Look for parasitized red blood cells.
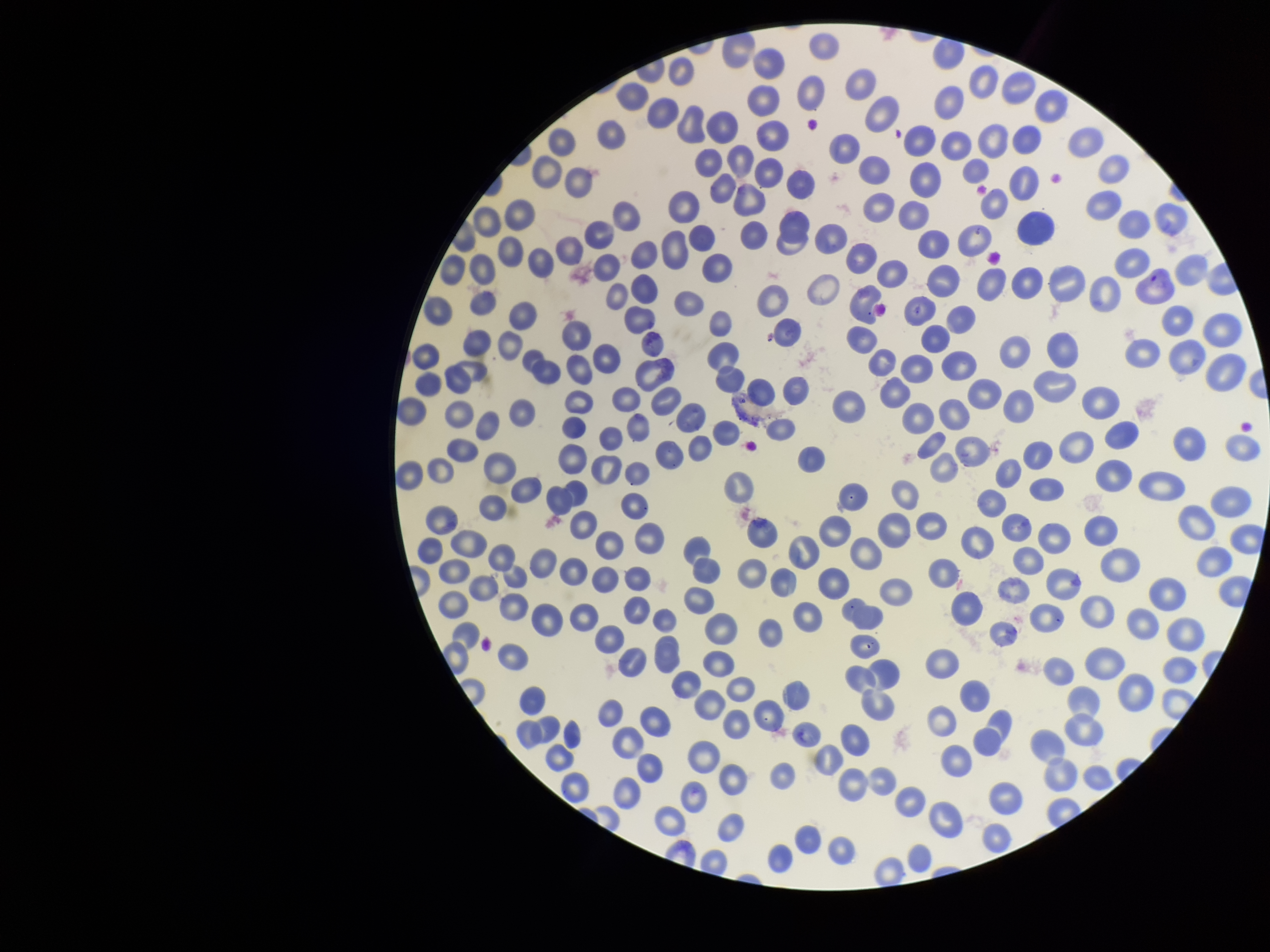

None seen.

Red blood cell count: 277. Patient malaria status: infected. Parasitized red blood cell count: 0. Species reported for this patient: Plasmodium vivax. Image is 1270×952 pixels. Photographed through the microscope eyepiece with a smartphone camera. One field from this slide. Stained with Giemsa. Preparation: thin smear.